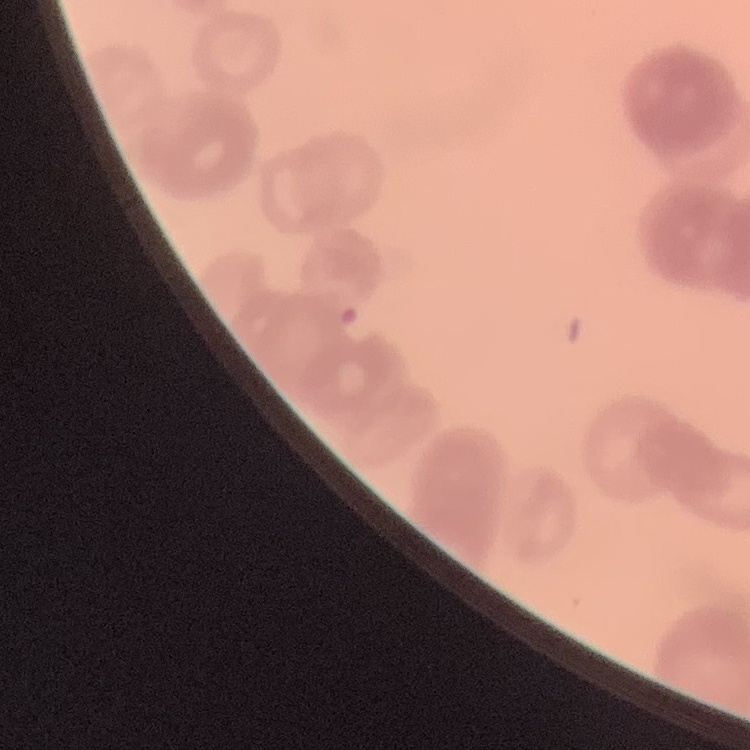

erythrocyte morphology = rouleaux formation
preparation = thin blood smear
stain = Field's or Giemsa
image type = square crop of a larger photomicrograph